Assess the morphology of the erythrocytes.
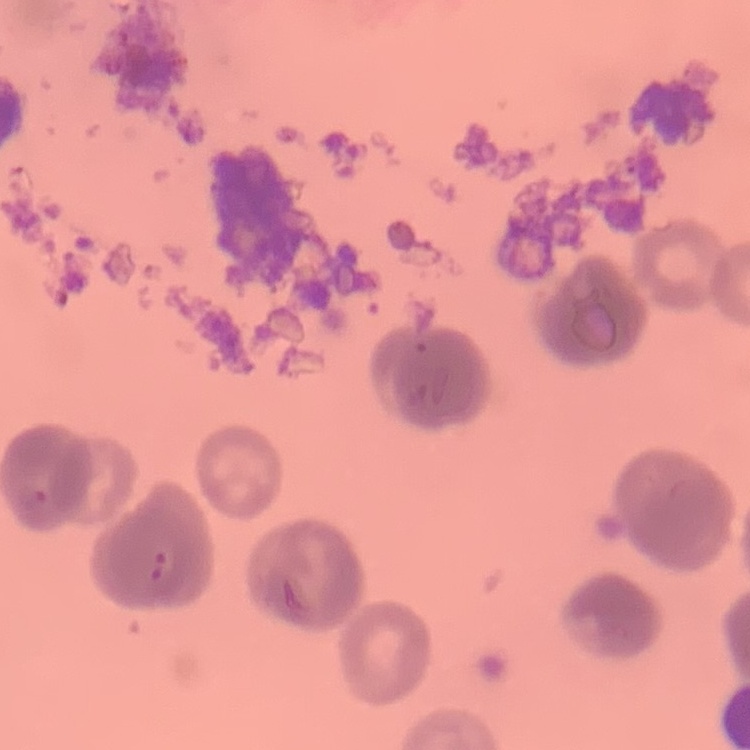

Rouleaux formation.

{
  "stain": "Field's or Giemsa",
  "preparation": "thin blood film",
  "image_type": "one tile cut from a larger photomicrograph"
}